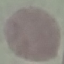

Malaria status: uninfected. Acquired by smartphone through the microscope eyepiece. Giemsa stain. Automatically extracted cell patch, resized to 64 × 64 pixels. Thin blood smear.